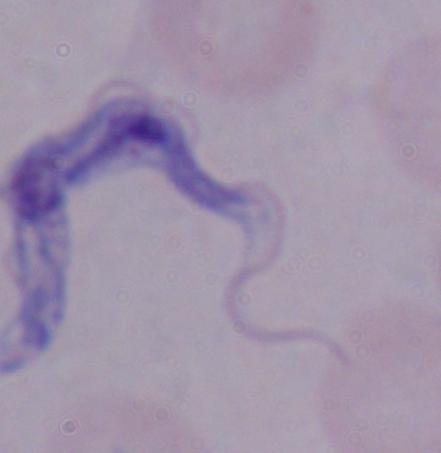

Photomicrograph. Captured at 1000x magnification. A trypanosome is shown.